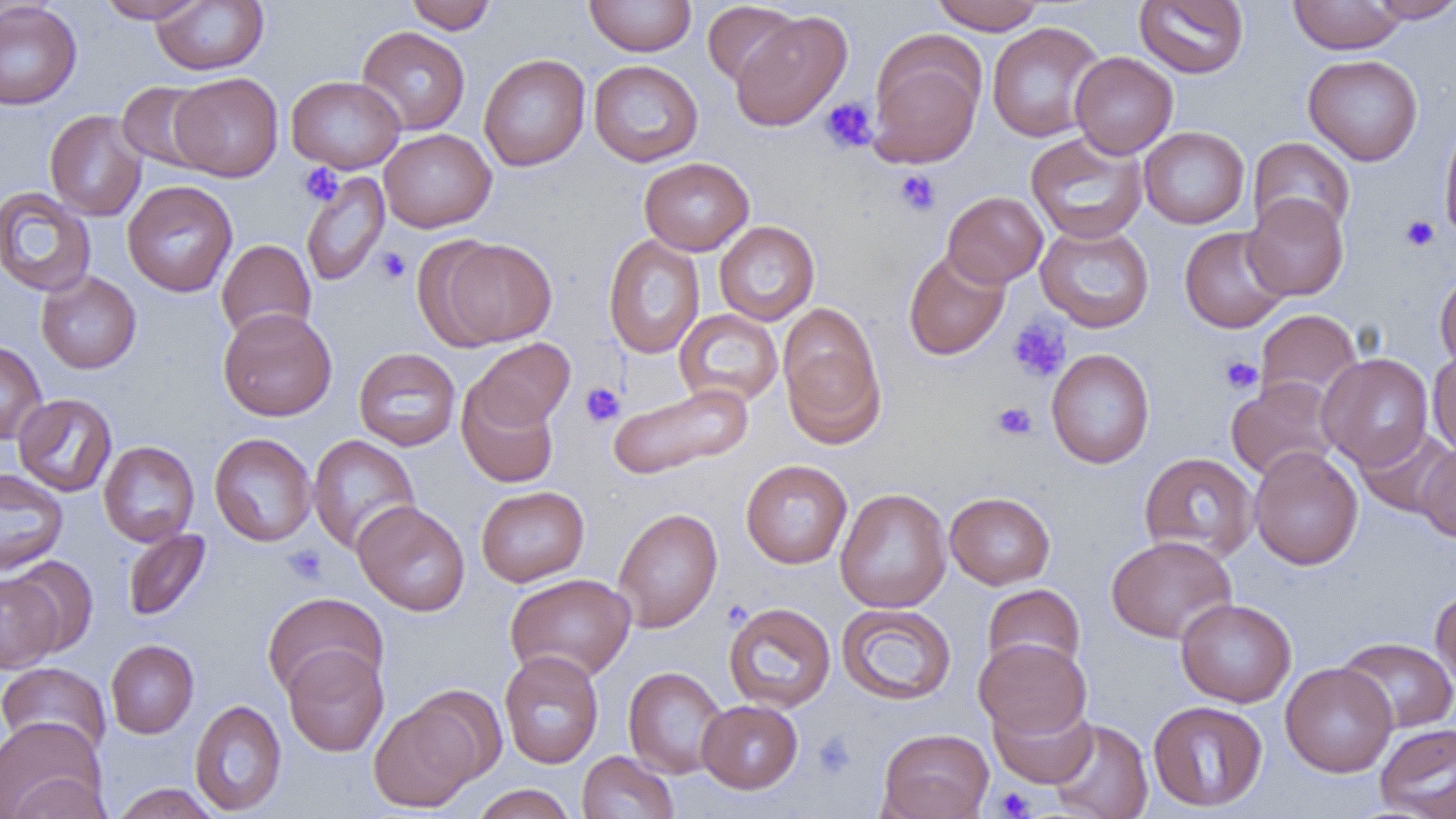
slide-level diagnosis = negative for blood parasites
image size = 1456×819 pixels
modality = light microscopy
field of view = single
platelet locations = approximate bounding boxes as named x1/y1/x2/y2 corners in pixels: (x1=820, y1=97, x2=879, y2=154), (x1=300, y1=163, x2=343, y2=205), (x1=894, y1=168, x2=941, y2=216), (x1=1400, y1=215, x2=1440, y2=252), (x1=375, y1=247, x2=411, y2=284), (x1=1007, y1=317, x2=1072, y2=384), (x1=1219, y1=355, x2=1263, y2=394), (x1=580, y1=382, x2=625, y2=427), (x1=992, y1=401, x2=1037, y2=441), (x1=283, y1=544, x2=328, y2=584), (x1=812, y1=731, x2=856, y2=778), (x1=994, y1=787, x2=1037, y2=818)
uninfected red blood cell locations = approximate bounding boxes as named x1/y1/x2/y2 corners in pixels: (x1=96, y1=0, x2=207, y2=23), (x1=405, y1=0, x2=498, y2=34), (x1=584, y1=0, x2=696, y2=56), (x1=930, y1=0, x2=1046, y2=34), (x1=1288, y1=0, x2=1405, y2=53), (x1=1366, y1=0, x2=1456, y2=24), (x1=151, y1=1, x2=269, y2=75), (x1=1134, y1=1, x2=1249, y2=78), (x1=0, y1=2, x2=83, y2=110), (x1=702, y1=2, x2=801, y2=88), (x1=729, y1=10, x2=852, y2=132), (x1=986, y1=21, x2=1106, y2=143), (x1=356, y1=26, x2=470, y2=135), (x1=869, y1=29, x2=1107, y2=154), (x1=868, y1=36, x2=985, y2=169), (x1=1069, y1=51, x2=1178, y2=158), (x1=478, y1=54, x2=590, y2=171), (x1=1303, y1=54, x2=1423, y2=166), (x1=589, y1=60, x2=703, y2=166), (x1=170, y1=73, x2=283, y2=181), (x1=286, y1=75, x2=405, y2=173), (x1=116, y1=81, x2=216, y2=173), (x1=44, y1=110, x2=147, y2=221), (x1=1439, y1=115, x2=1456, y2=244), (x1=1138, y1=126, x2=1250, y2=229), (x1=379, y1=128, x2=496, y2=233), (x1=1025, y1=132, x2=1148, y2=244), (x1=1248, y1=137, x2=1355, y2=239), (x1=639, y1=157, x2=754, y2=255), (x1=301, y1=170, x2=391, y2=286), (x1=122, y1=180, x2=237, y2=297), (x1=0, y1=187, x2=96, y2=297), (x1=941, y1=191, x2=1048, y2=288), (x1=1243, y1=194, x2=1349, y2=301), (x1=714, y1=221, x2=820, y2=325), (x1=1035, y1=223, x2=1154, y2=332), (x1=1179, y1=226, x2=1290, y2=333), (x1=603, y1=235, x2=705, y2=359), (x1=433, y1=237, x2=557, y2=347), (x1=216, y1=239, x2=316, y2=342), (x1=903, y1=249, x2=1011, y2=361), (x1=1435, y1=269, x2=1456, y2=373), (x1=36, y1=271, x2=141, y2=374), (x1=778, y1=303, x2=886, y2=446), (x1=217, y1=307, x2=337, y2=421), (x1=674, y1=309, x2=784, y2=407), (x1=1255, y1=309, x2=1362, y2=408), (x1=471, y1=338, x2=575, y2=431), (x1=0, y1=339, x2=47, y2=445), (x1=353, y1=347, x2=461, y2=451), (x1=1046, y1=348, x2=1155, y2=469), (x1=1428, y1=349, x2=1456, y2=458), (x1=1318, y1=353, x2=1433, y2=470), (x1=1225, y1=377, x2=1341, y2=481), (x1=457, y1=380, x2=559, y2=489), (x1=608, y1=383, x2=753, y2=480), (x1=13, y1=393, x2=117, y2=497), (x1=1354, y1=425, x2=1455, y2=518), (x1=209, y1=433, x2=317, y2=546), (x1=308, y1=435, x2=420, y2=555), (x1=99, y1=441, x2=200, y2=546), (x1=1416, y1=442, x2=1456, y2=542), (x1=1249, y1=446, x2=1363, y2=570), (x1=1138, y1=451, x2=1259, y2=563), (x1=741, y1=459, x2=852, y2=568), (x1=0, y1=468, x2=68, y2=576), (x1=476, y1=485, x2=589, y2=586), (x1=835, y1=488, x2=951, y2=613), (x1=945, y1=492, x2=1056, y2=589), (x1=352, y1=500, x2=470, y2=616), (x1=612, y1=507, x2=723, y2=632), (x1=122, y1=527, x2=213, y2=623), (x1=1106, y1=534, x2=1237, y2=644), (x1=8, y1=556, x2=98, y2=658), (x1=0, y1=573, x2=63, y2=673), (x1=505, y1=573, x2=636, y2=682), (x1=982, y1=583, x2=1086, y2=678), (x1=1431, y1=587, x2=1456, y2=695), (x1=262, y1=592, x2=387, y2=699), (x1=1176, y1=598, x2=1296, y2=707), (x1=723, y1=602, x2=836, y2=713), (x1=836, y1=603, x2=957, y2=705), (x1=1335, y1=636, x2=1456, y2=734), (x1=974, y1=638, x2=1092, y2=740), (x1=105, y1=639, x2=199, y2=738), (x1=283, y1=647, x2=389, y2=756), (x1=499, y1=651, x2=605, y2=768), (x1=0, y1=662, x2=111, y2=759), (x1=1280, y1=662, x2=1397, y2=777), (x1=623, y1=666, x2=729, y2=779), (x1=368, y1=695, x2=486, y2=812), (x1=989, y1=696, x2=1097, y2=788), (x1=189, y1=699, x2=287, y2=816), (x1=697, y1=699, x2=803, y2=794), (x1=1147, y1=700, x2=1268, y2=812), (x1=0, y1=717, x2=106, y2=819), (x1=1047, y1=718, x2=1153, y2=819), (x1=1374, y1=723, x2=1456, y2=819), (x1=877, y1=728, x2=994, y2=819), (x1=577, y1=751, x2=678, y2=818), (x1=5, y1=773, x2=112, y2=818), (x1=110, y1=783, x2=221, y2=819), (x1=472, y1=784, x2=577, y2=819)
magnification = 1000x
preparation = thin blood smear